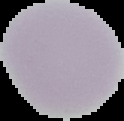
preparation: thin blood film
result: no Plasmodium parasites seen
image_size: 124×121 pixels
image_type: cell region segmented out of the field of view; surrounding area masked to black